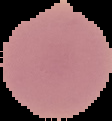
{
  "preparation": "thin blood smear",
  "malaria_status": "uninfected",
  "image_size": "112×121 pixels",
  "image_type": "cell region segmented out of the field of view; surrounding area masked to black"
}